Report the malaria status of this cell.
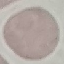
It is uninfected.

Giemsa-stained preparation. Thin blood film. Automatically extracted cell patch, resized to 64 × 64 pixels. Photographed with a smartphone camera at the microscope eyepiece.